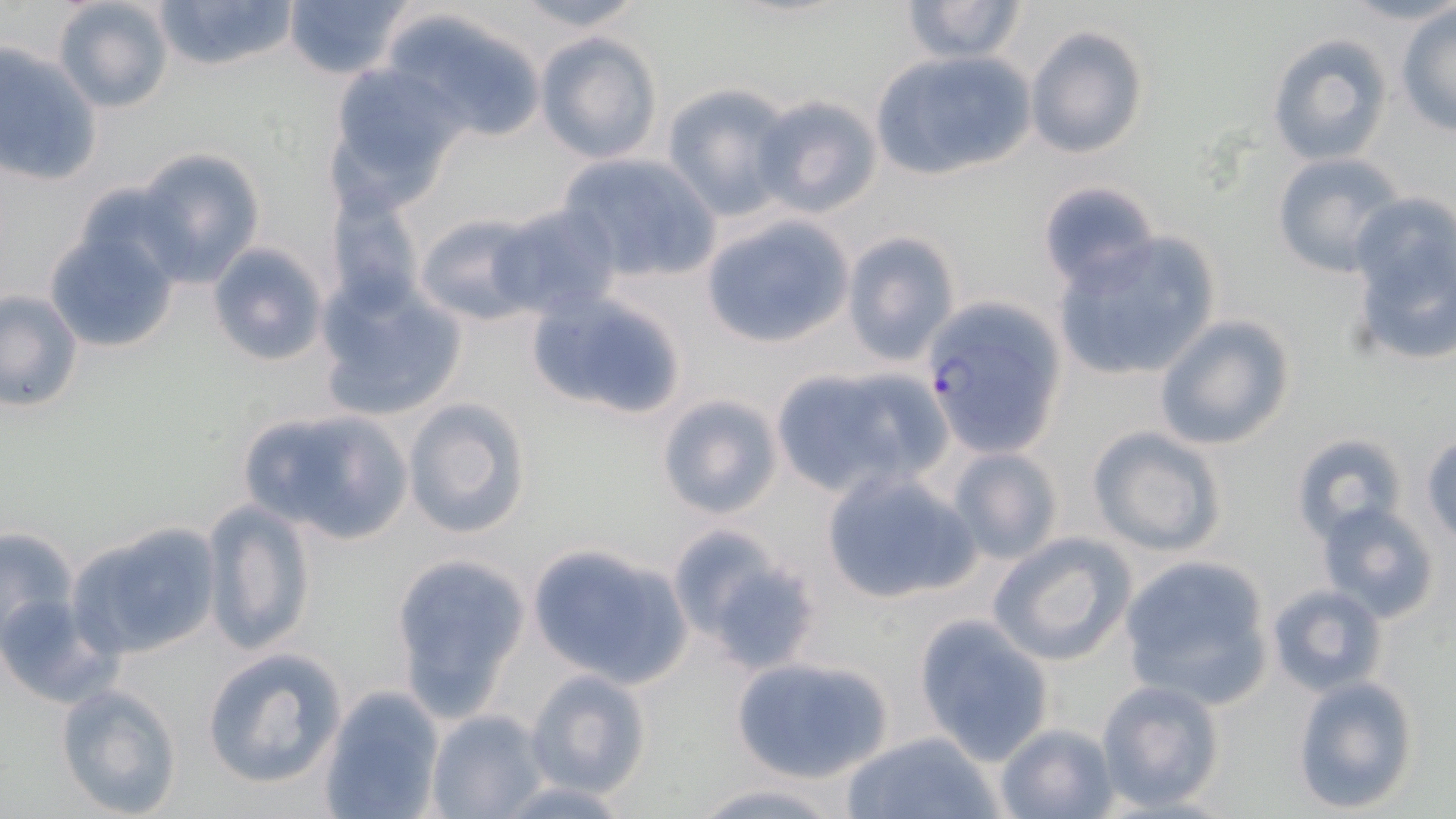
slide_level_diagnosis: Plasmodium falciparum
image_size: 1456×819 pixels
preparation: thin blood film
uninfected_red_blood_cell_locations: 'approximate bounding boxes as named x1/y1/x2/y2 corners in pixels: (x1=52, y1=0, x2=175, y2=114), (x1=152, y1=0, x2=298, y2=75), (x1=283, y1=0, x2=411, y2=81), (x1=507, y1=0, x2=648, y2=31), (x1=899, y1=0, x2=1030, y2=64), (x1=1395, y1=6, x2=1456, y2=137), (x1=383, y1=7, x2=549, y2=143), (x1=1024, y1=26, x2=1149, y2=159), (x1=535, y1=31, x2=663, y2=164), (x1=1267, y1=34, x2=1392, y2=166), (x1=0, y1=42, x2=102, y2=187), (x1=867, y1=50, x2=1038, y2=182), (x1=325, y1=61, x2=466, y2=201), (x1=660, y1=85, x2=795, y2=218), (x1=753, y1=93, x2=883, y2=217), (x1=133, y1=148, x2=268, y2=286), (x1=555, y1=152, x2=720, y2=283), (x1=1269, y1=152, x2=1406, y2=279), (x1=1038, y1=181, x2=1160, y2=293), (x1=1344, y1=194, x2=1456, y2=370), (x1=327, y1=195, x2=424, y2=309), (x1=491, y1=203, x2=623, y2=321), (x1=414, y1=211, x2=546, y2=326), (x1=699, y1=211, x2=856, y2=351), (x1=45, y1=227, x2=179, y2=352), (x1=840, y1=232, x2=960, y2=366), (x1=1051, y1=232, x2=1222, y2=384), (x1=207, y1=243, x2=328, y2=365), (x1=317, y1=273, x2=468, y2=418), (x1=1, y1=289, x2=82, y2=411), (x1=526, y1=291, x2=689, y2=424), (x1=1153, y1=312, x2=1298, y2=450), (x1=766, y1=362, x2=950, y2=498), (x1=655, y1=395, x2=783, y2=520), (x1=402, y1=396, x2=531, y2=540), (x1=237, y1=406, x2=413, y2=547), (x1=1086, y1=426, x2=1227, y2=557), (x1=1291, y1=433, x2=1411, y2=544), (x1=1420, y1=434, x2=1456, y2=546), (x1=944, y1=447, x2=1065, y2=565), (x1=822, y1=469, x2=981, y2=604), (x1=201, y1=498, x2=316, y2=657), (x1=1314, y1=502, x2=1442, y2=623), (x1=69, y1=521, x2=222, y2=661), (x1=0, y1=525, x2=81, y2=650), (x1=672, y1=530, x2=825, y2=674), (x1=990, y1=531, x2=1138, y2=667), (x1=525, y1=544, x2=692, y2=687), (x1=1117, y1=554, x2=1275, y2=708), (x1=391, y1=556, x2=528, y2=712), (x1=1266, y1=582, x2=1389, y2=696), (x1=0, y1=595, x2=114, y2=707), (x1=913, y1=614, x2=1055, y2=764), (x1=202, y1=647, x2=344, y2=788), (x1=730, y1=655, x2=895, y2=784), (x1=523, y1=669, x2=652, y2=799), (x1=1290, y1=673, x2=1421, y2=814), (x1=1093, y1=678, x2=1227, y2=811), (x1=56, y1=682, x2=184, y2=817), (x1=321, y1=686, x2=445, y2=819), (x1=427, y1=709, x2=548, y2=818), (x1=994, y1=722, x2=1118, y2=819), (x1=842, y1=729, x2=1002, y2=819), (x1=684, y1=781, x2=850, y2=818)'
plasmodium_falciparum_infected_red_blood_cell_locations: 'approximate bounding boxes as named x1/y1/x2/y2 corners in pixels: (x1=919, y1=296, x2=1068, y2=456)'
field_of_view: one of a larger specimen
modality: optical microscopy
magnification: 1000x
stain: May-Grünwald-Giemsa